Find each white blood cell.
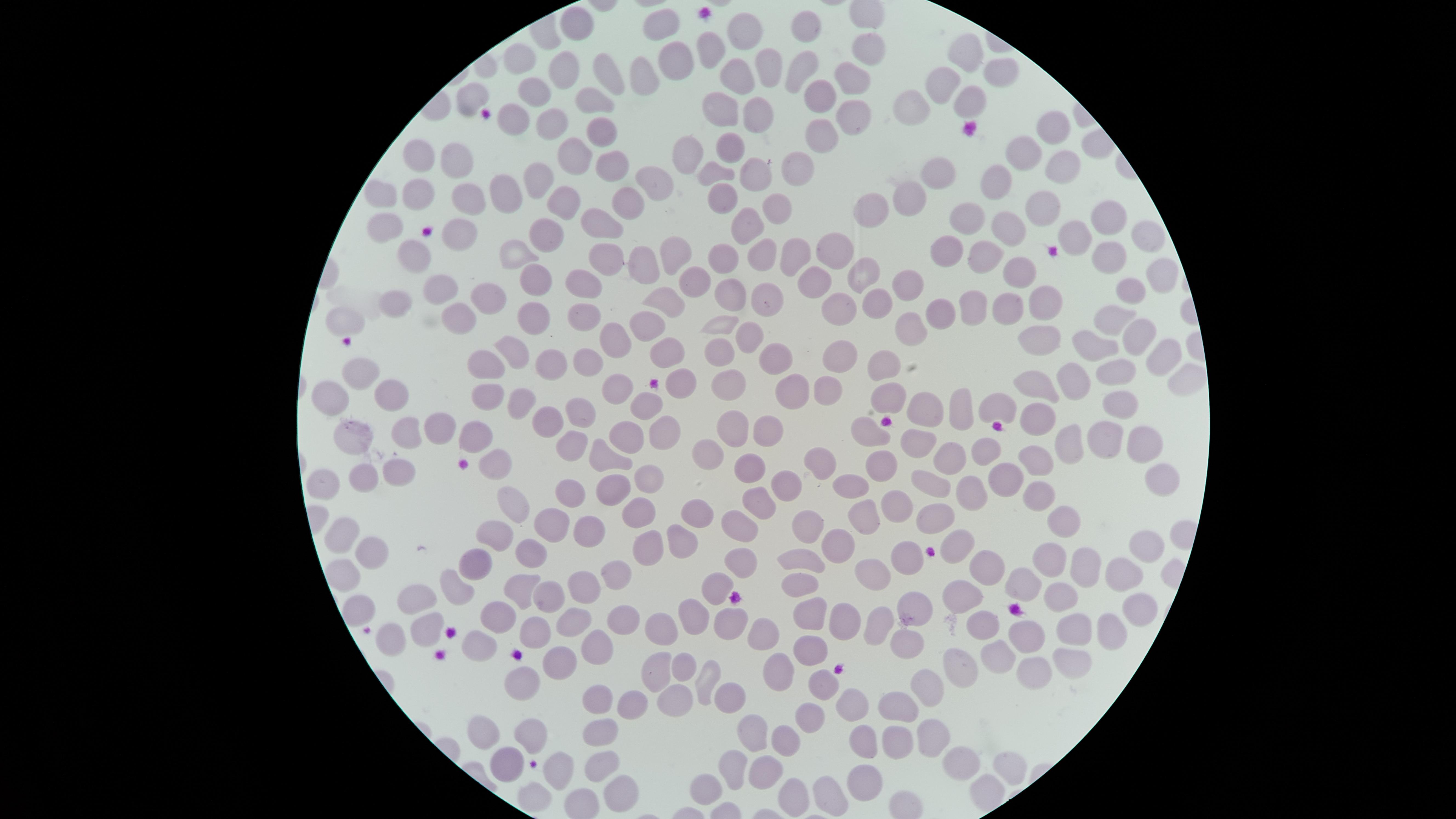
No white blood cells identified.

Approximate marker points, in pixels from the top-left corner.
Summary:
  - Uninfected red blood cells: (x=661, y=20), (x=576, y=22), (x=734, y=32), (x=810, y=32), (x=867, y=46), (x=709, y=47), (x=522, y=50), (x=965, y=50), (x=671, y=57), (x=565, y=61), (x=801, y=64), (x=765, y=66), (x=597, y=69), (x=734, y=69), (x=1004, y=71), (x=642, y=77), (x=849, y=77), (x=938, y=84), (x=813, y=88), (x=534, y=94), (x=597, y=94), (x=969, y=96), (x=472, y=99), (x=913, y=107), (x=715, y=110), (x=753, y=110), (x=846, y=111), (x=509, y=113), (x=548, y=117), (x=1048, y=127), (x=602, y=128), (x=817, y=139), (x=726, y=145), (x=413, y=150), (x=1017, y=152), (x=571, y=154), (x=688, y=154), (x=458, y=159), (x=606, y=161), (x=713, y=167), (x=1057, y=167), (x=756, y=169), (x=794, y=169), (x=935, y=173), (x=654, y=174), (x=991, y=183), (x=538, y=184), (x=382, y=190), (x=416, y=190), (x=725, y=190), (x=465, y=193), (x=505, y=193), (x=625, y=196), (x=908, y=199), (x=563, y=202), (x=870, y=205), (x=775, y=209), (x=1040, y=211), (x=965, y=215), (x=606, y=217), (x=1105, y=218), (x=378, y=224), (x=456, y=227), (x=747, y=227), (x=1001, y=230), (x=1075, y=230), (x=544, y=232), (x=1151, y=236), (x=825, y=247), (x=518, y=249), (x=678, y=250), (x=983, y=251), (x=786, y=252), (x=409, y=253), (x=945, y=253), (x=758, y=254), (x=1104, y=256), (x=603, y=261), (x=715, y=262), (x=642, y=263), (x=1021, y=268), (x=865, y=273), (x=1156, y=273), (x=532, y=275), (x=904, y=280), (x=813, y=281), (x=581, y=284), (x=694, y=288), (x=440, y=290), (x=1121, y=292), (x=481, y=293), (x=764, y=297), (x=726, y=299), (x=393, y=300), (x=1041, y=300), (x=871, y=303), (x=664, y=304), (x=833, y=307), (x=1006, y=308), (x=970, y=309), (x=936, y=310), (x=538, y=312), (x=579, y=313), (x=1112, y=315), (x=342, y=319), (x=453, y=320), (x=647, y=325), (x=719, y=325), (x=905, y=326), (x=751, y=329), (x=1136, y=334), (x=1049, y=337), (x=607, y=340), (x=1097, y=348), (x=516, y=349), (x=664, y=353), (x=1162, y=353), (x=772, y=354), (x=834, y=354), (x=716, y=355), (x=586, y=360), (x=487, y=362), (x=548, y=362), (x=881, y=366), (x=1122, y=368), (x=361, y=372), (x=1076, y=374), (x=680, y=377), (x=1181, y=379), (x=730, y=381), (x=1031, y=381), (x=397, y=387), (x=483, y=391), (x=617, y=391), (x=785, y=391), (x=824, y=391), (x=887, y=393), (x=329, y=396), (x=525, y=397), (x=994, y=402), (x=647, y=403), (x=922, y=403), (x=961, y=403), (x=1120, y=405), (x=577, y=414), (x=1035, y=414), (x=732, y=422), (x=768, y=426), (x=432, y=429), (x=666, y=430), (x=867, y=431), (x=403, y=432), (x=476, y=435), (x=350, y=436), (x=630, y=436), (x=918, y=437), (x=1100, y=438), (x=1139, y=441), (x=568, y=444), (x=1063, y=445), (x=707, y=451), (x=982, y=451), (x=604, y=452), (x=948, y=456), (x=1038, y=457), (x=495, y=461), (x=819, y=461), (x=878, y=464), (x=751, y=467), (x=395, y=471), (x=1006, y=473), (x=322, y=474), (x=362, y=476), (x=1155, y=476), (x=649, y=477), (x=927, y=479), (x=787, y=483), (x=973, y=487), (x=606, y=488), (x=844, y=488), (x=567, y=489), (x=574, y=489), (x=1041, y=494), (x=758, y=496), (x=511, y=498), (x=899, y=502), (x=636, y=513), (x=930, y=514), (x=701, y=516), (x=862, y=516), (x=812, y=517), (x=734, y=518), (x=1058, y=518), (x=545, y=526), (x=585, y=530), (x=491, y=534), (x=341, y=535), (x=683, y=537), (x=834, y=542), (x=949, y=542), (x=1143, y=546), (x=644, y=548), (x=367, y=549), (x=533, y=554), (x=904, y=554), (x=1048, y=556), (x=798, y=559), (x=745, y=561), (x=977, y=563), (x=1080, y=563), (x=476, y=564), (x=342, y=568), (x=873, y=569), (x=615, y=570), (x=1119, y=570), (x=581, y=581), (x=1021, y=581), (x=453, y=583), (x=722, y=584), (x=522, y=586), (x=797, y=586), (x=549, y=596), (x=1063, y=596), (x=957, y=597), (x=418, y=599), (x=912, y=602), (x=356, y=605), (x=814, y=611), (x=697, y=612), (x=1138, y=612), (x=576, y=615), (x=501, y=616), (x=623, y=618), (x=730, y=619), (x=842, y=619), (x=987, y=620), (x=528, y=622), (x=664, y=624), (x=881, y=624), (x=1073, y=628), (x=424, y=629), (x=1109, y=629), (x=754, y=633), (x=1032, y=633), (x=388, y=636), (x=475, y=641), (x=806, y=643), (x=597, y=645), (x=997, y=650), (x=1070, y=659), (x=552, y=662), (x=682, y=662), (x=958, y=663), (x=659, y=667), (x=774, y=669), (x=523, y=671), (x=1029, y=672), (x=702, y=674), (x=931, y=687), (x=815, y=688), (x=681, y=695), (x=727, y=695), (x=595, y=702), (x=904, y=702), (x=852, y=703), (x=628, y=710), (x=803, y=720), (x=755, y=729), (x=484, y=730), (x=598, y=733), (x=530, y=737), (x=937, y=737), (x=896, y=738), (x=783, y=740), (x=862, y=744), (x=558, y=762), (x=737, y=762), (x=961, y=762), (x=504, y=764), (x=1008, y=764), (x=605, y=766), (x=768, y=767), (x=862, y=775), (x=706, y=778), (x=617, y=786), (x=796, y=786), (x=827, y=787), (x=533, y=792)
  - Presence: no malaria parasites detected
  - Stain: Giemsa
  - Preparation: thin blood film
  - Capture: smartphone photograph through the microscope eyepiece
  - Field of view: single
  - Visible region: circular
  - Image size: 1456×819 pixels